Classify this cell by malaria status.
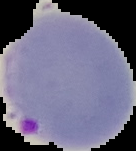

Parasitized.

Summary:
  - Preparation: thin blood smear
  - Image size: 136×151 pixels
  - Image type: segmented cell region with the area outside set to black